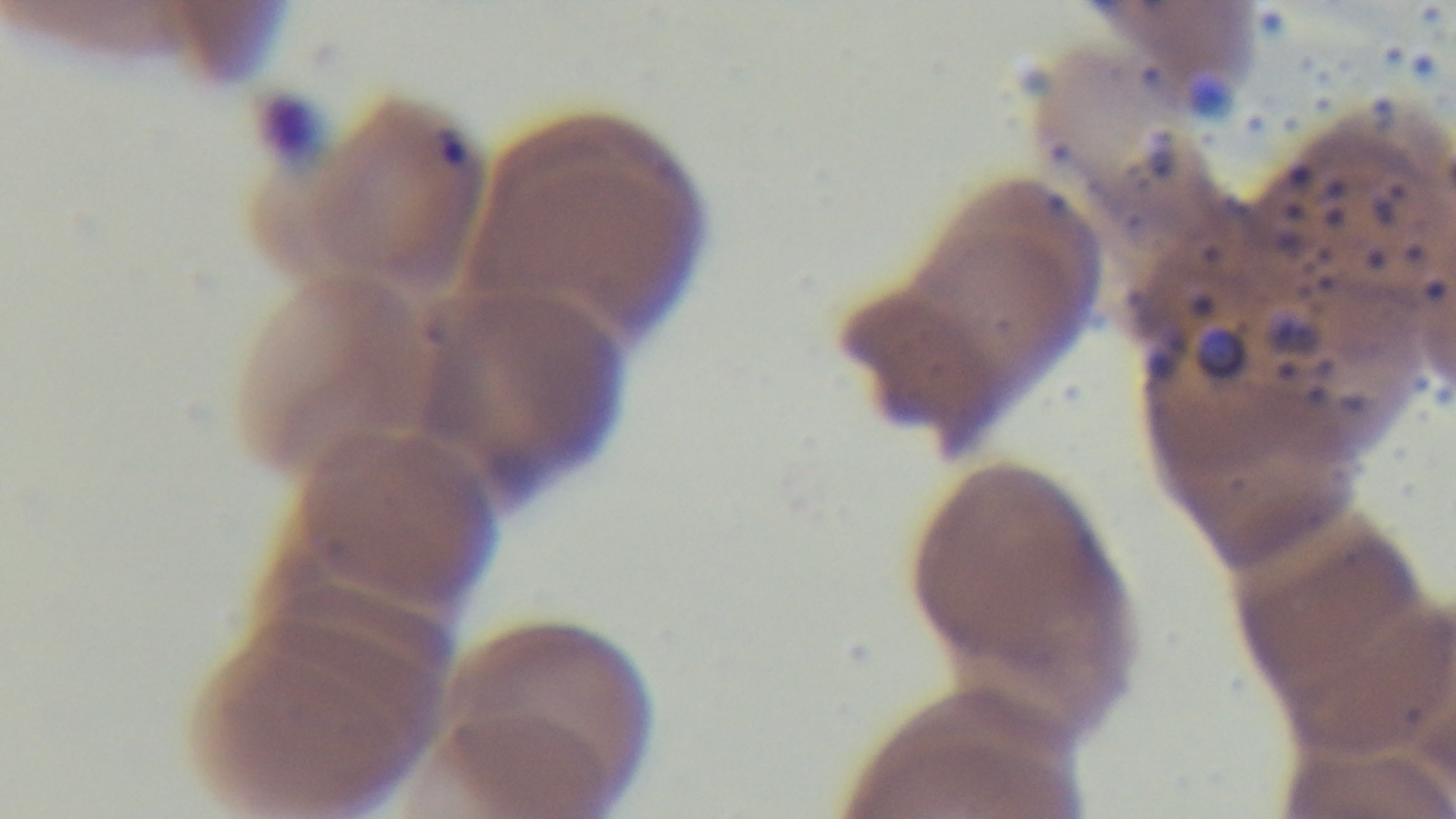

malaria_status: positive
capture: mounted 4K digital camera
stain: Giemsa
preparation: thin smear
modality: light microscopy
field_of_view: single
objective: 100x oil immersion